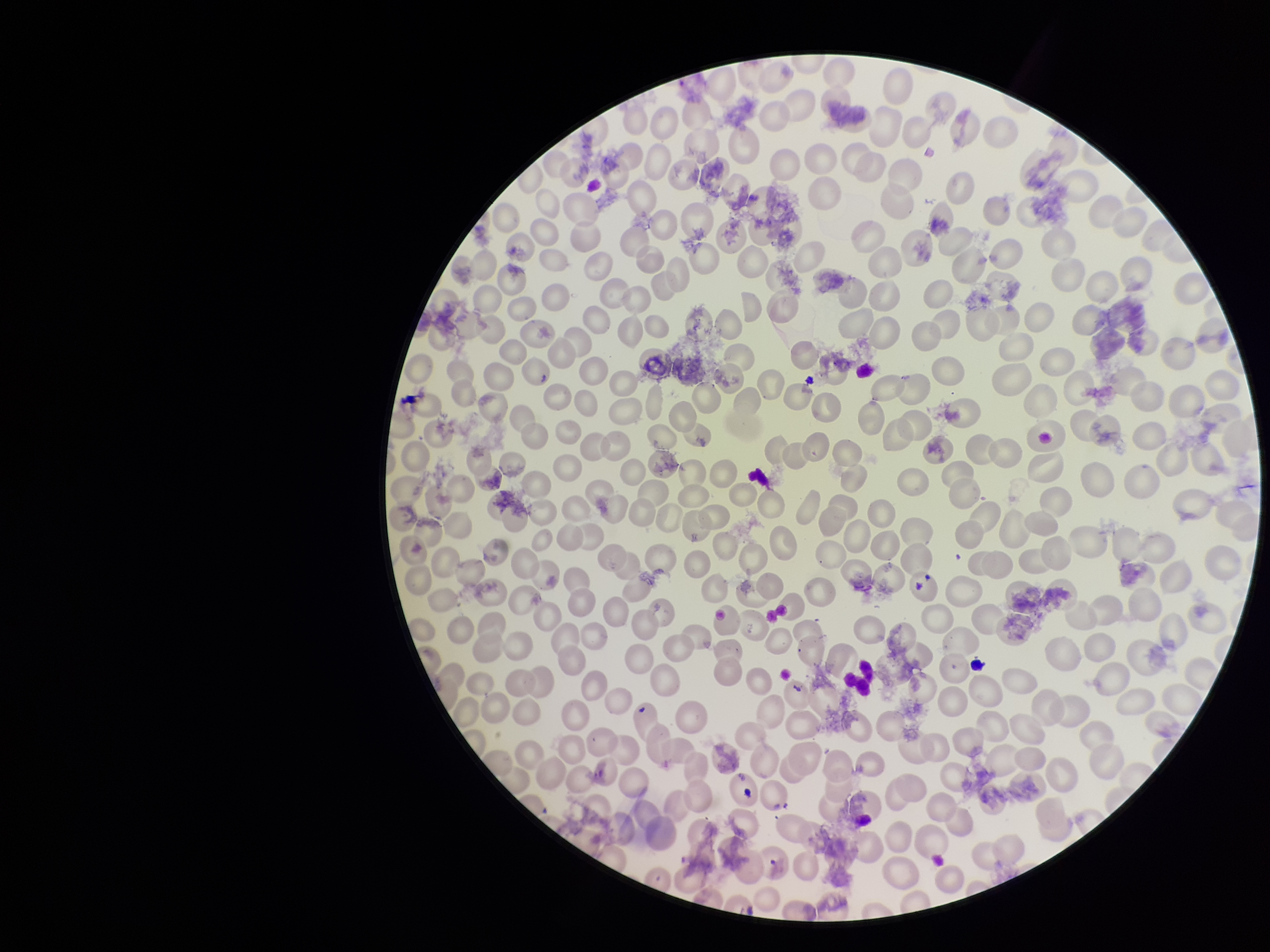
Summary:
  - Preparation: thin blood smear
  - Patient malaria status: positive
  - Red blood cell count: 241
  - Image size: 1270×952 pixels
  - Species reported for this patient: Plasmodium falciparum
  - Parasitized red blood cell count: 0
  - Field of view: one from this slide
  - Parasitized red blood cells: none detected
  - Capture: smartphone photograph through the microscope eyepiece
  - Stain: Giemsa